Describe the morphology of the red blood cells.
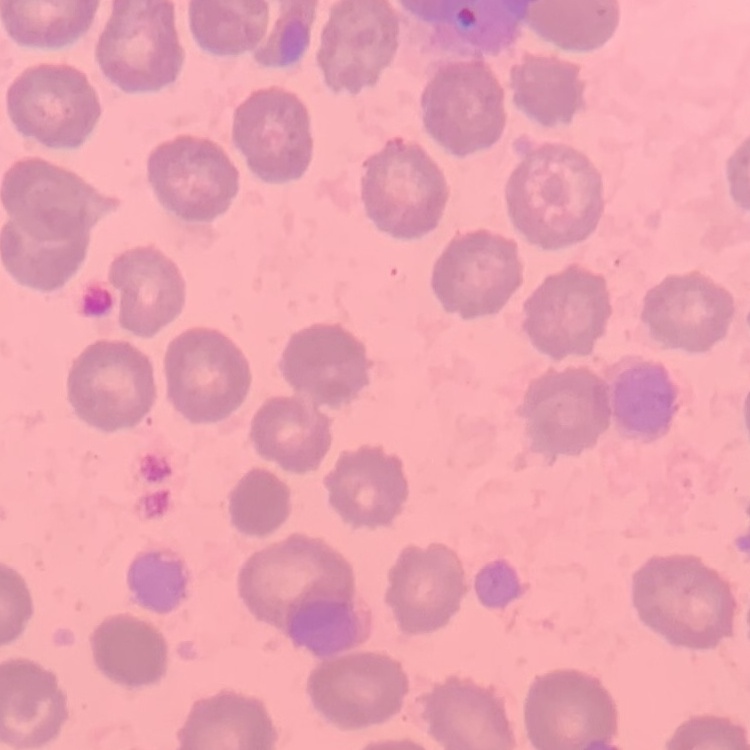
They show no rouleaux formation.

Summary:
  - Preparation: thin blood smear
  - Stain: Field's or Giemsa
  - Image type: square crop of a larger photomicrograph